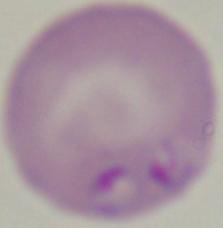
Summary:
  - Identification: Babesia
  - Magnification: 1000x
  - Modality: photomicrograph